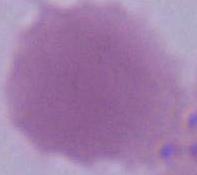

Summary:
  - Magnification: 1000x
  - Modality: photomicrograph
  - Identification: erythrocyte